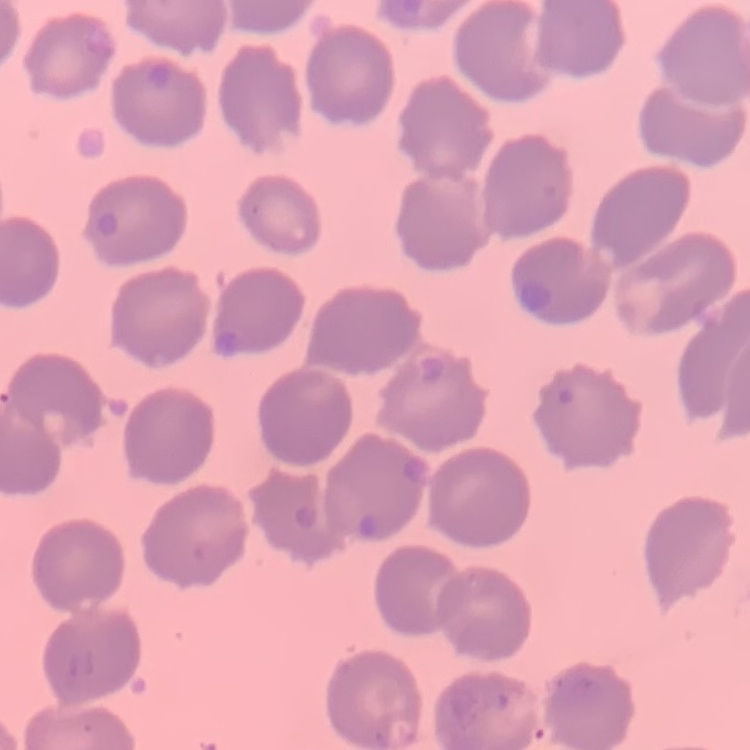 The red blood cells show no rouleaux formation. Square crop of a larger photomicrograph. Field's or Giemsa stain. Thin peripheral smear.